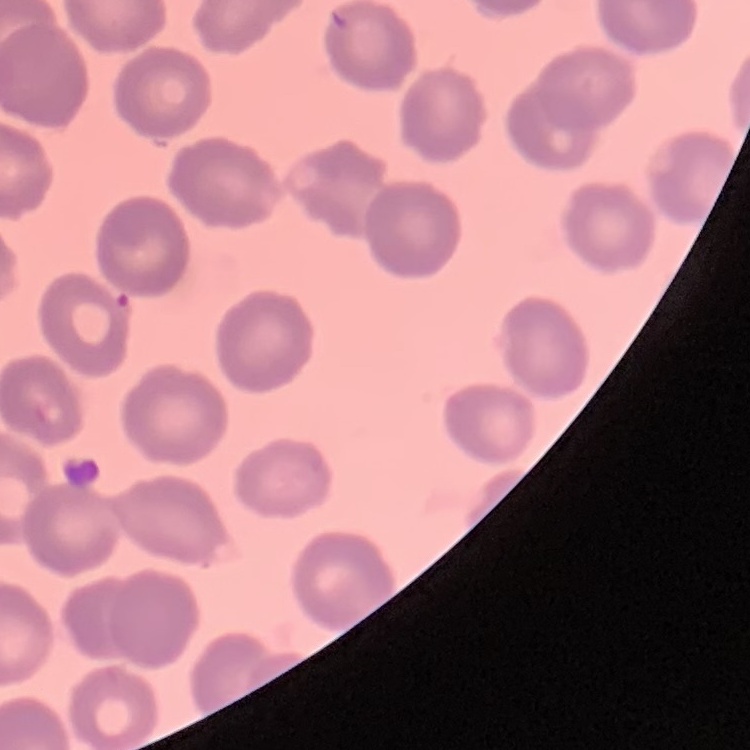
Summary:
  - Erythrocyte morphology: no rouleaux formation
  - Stain: Field's or Giemsa
  - Preparation: thin peripheral smear
  - Image type: one tile cut from a larger photomicrograph